Locate leukocytes (white blood cells).
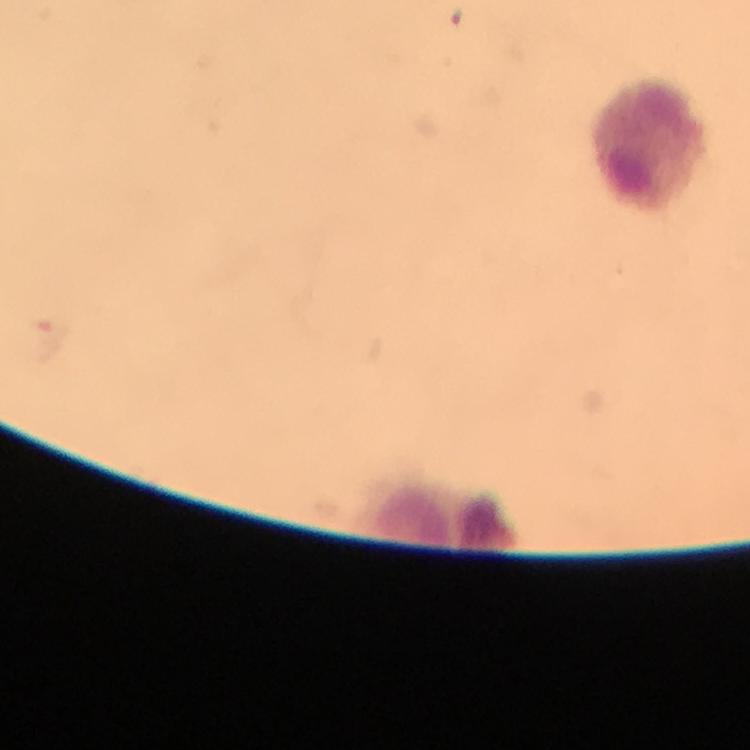

Approximate centers as {x, y} in pixels.
Leukocytes: {653, 142}, {444, 520}.

Summary:
  - Magnification: 100x
  - Cropped from: one field of view
  - Preparation: thick blood film
  - Stain: Giemsa
  - Image size: 750×750 pixels
  - Malaria parasites: none seen
  - Context: from a malaria diagnostic workup
  - Capture: smartphone mounted on the microscope
  - Immersion oil: applied